Report the malaria status.
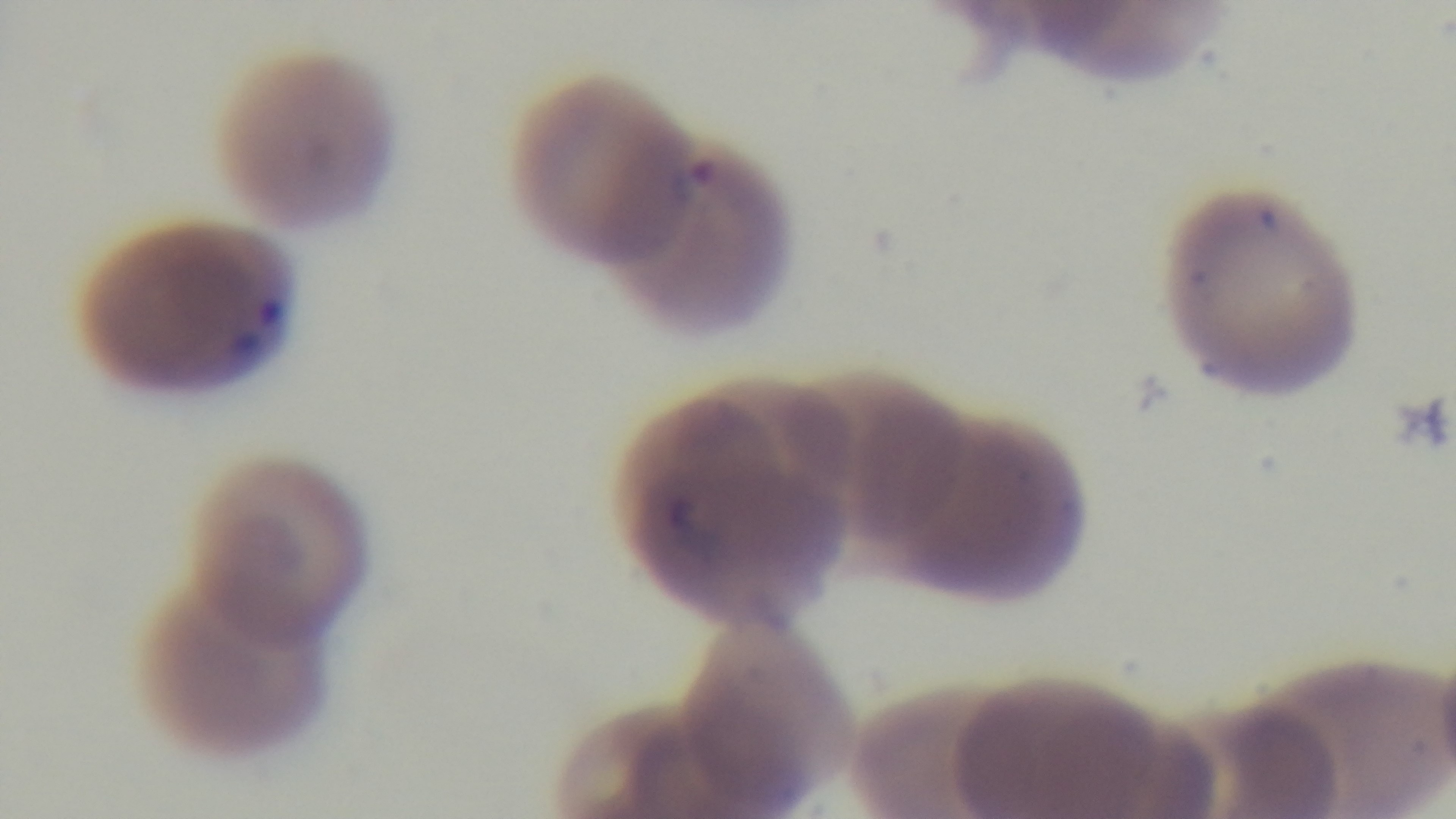

It is infected.

Summary:
  - Field of view: single
  - Capture: mounted 4K digital camera
  - Objective: 100x oil immersion
  - Modality: light microscopy
  - Stain: Giemsa
  - Preparation: thin smear